Give the preparation type.
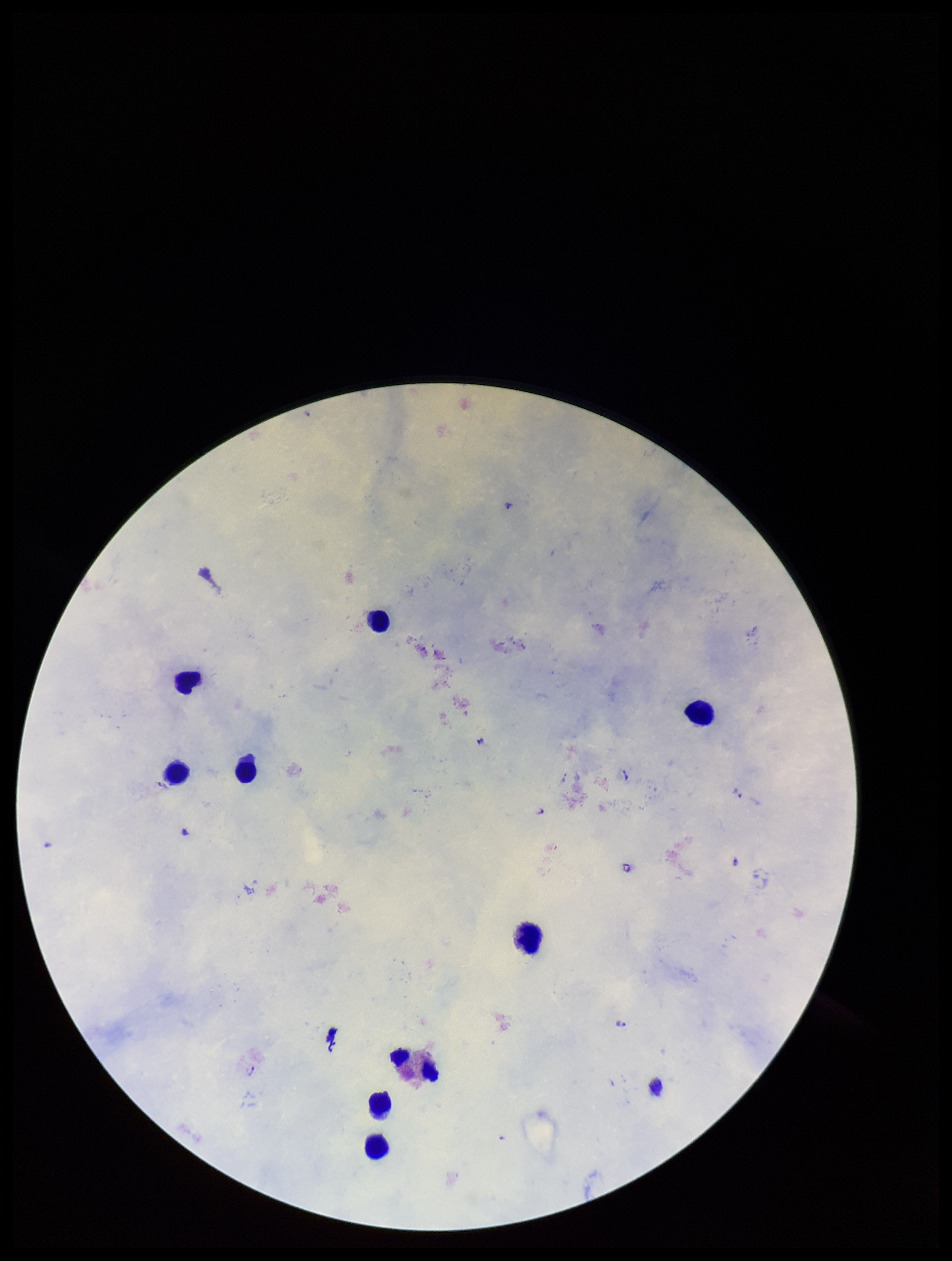
It is a thick blood smear.

Plasmodium parasites = seen
leukocyte count = 9
image size = 952×1261 pixels
species reported for this patient = Plasmodium falciparum
patient malaria status = positive
capture = smartphone photograph through the microscope eyepiece
parasite count = 5
stain = Giemsa
field of view = single